Identify the preparation type.
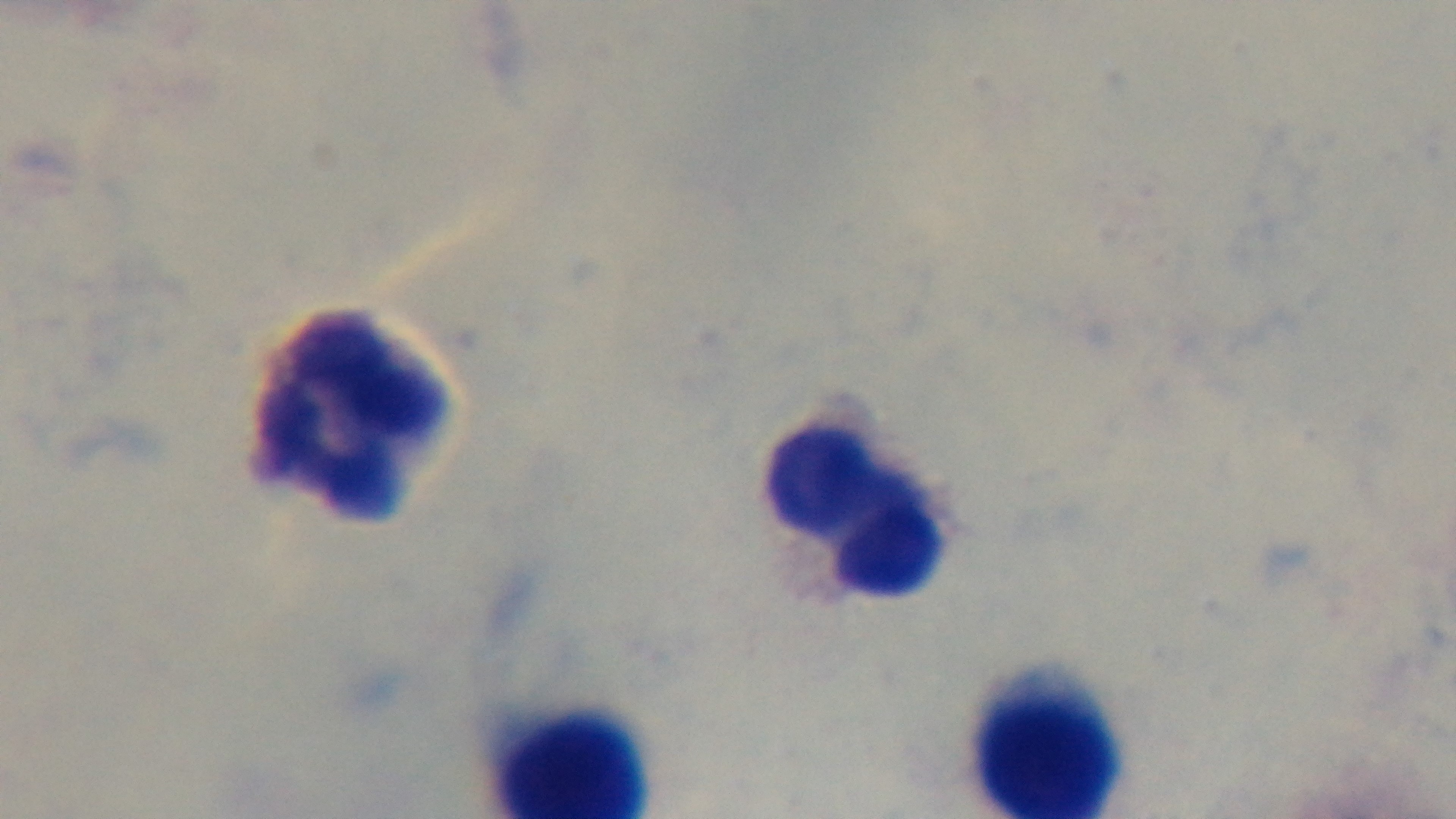

Thick.

Summary:
  - Objective: 100x oil immersion
  - Field of view: one from the slide
  - Stain: Giemsa
  - Capture: mounted 4K digital camera
  - Modality: light microscopy
  - Malaria status: negative